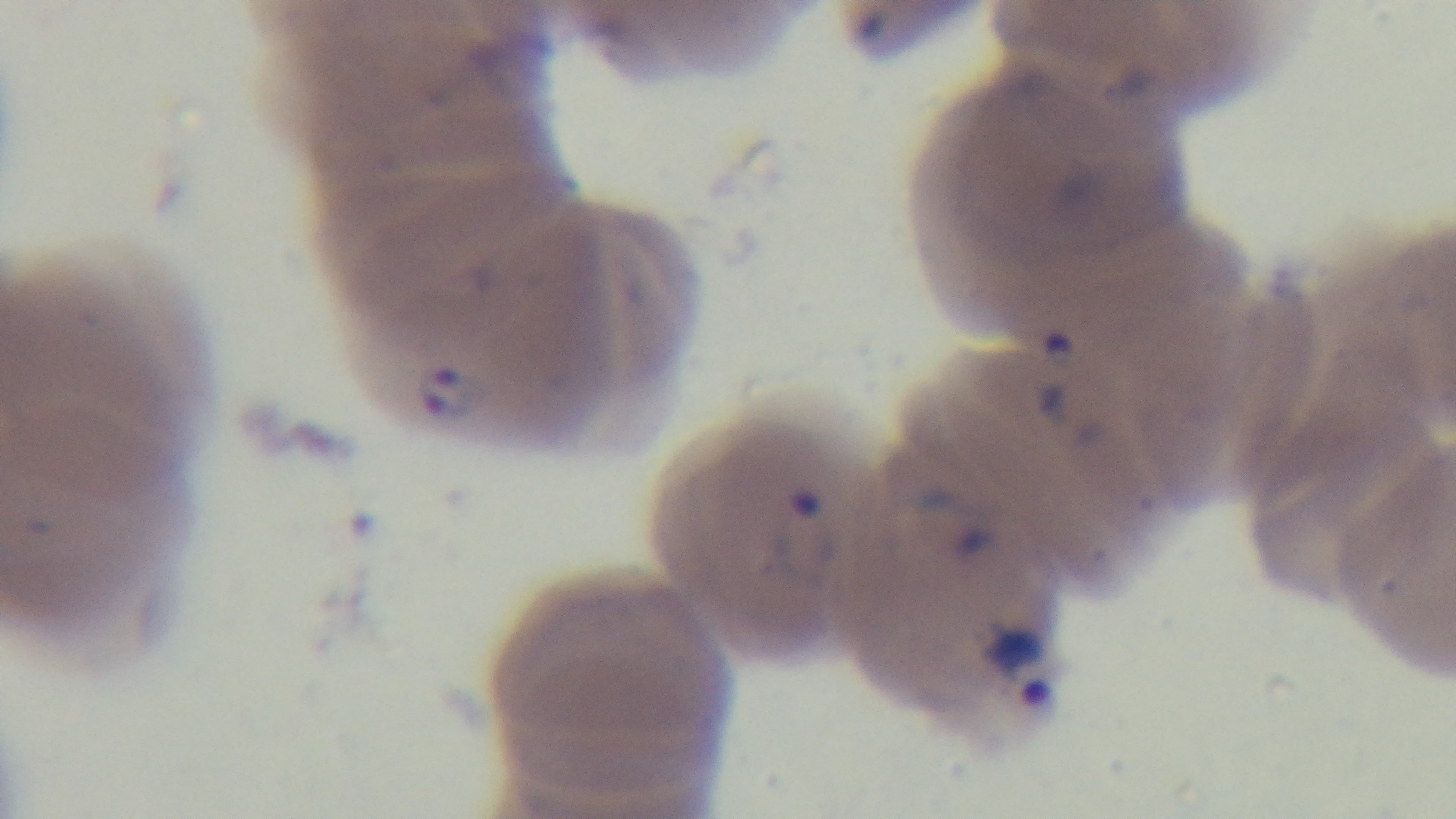

Photomicrograph. Preparation: thin blood film. Giemsa stain. 100x oil-immersion objective. Captured with a mounted 4K digital camera. One field from the slide. Malaria status: infected.